Report the malaria status of this cell.
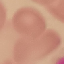

Uninfected.

preparation = thin blood film
image type = cell patch, automatically extracted from a larger field of view and resized to 64 × 64 pixels
capture = smartphone through the microscope eyepiece
stain = Giemsa